State which parasite is depicted.
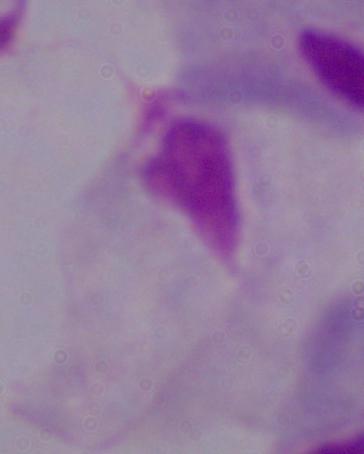
A trichomonad.

Summary:
  - Magnification: 1000x
  - Modality: micrograph